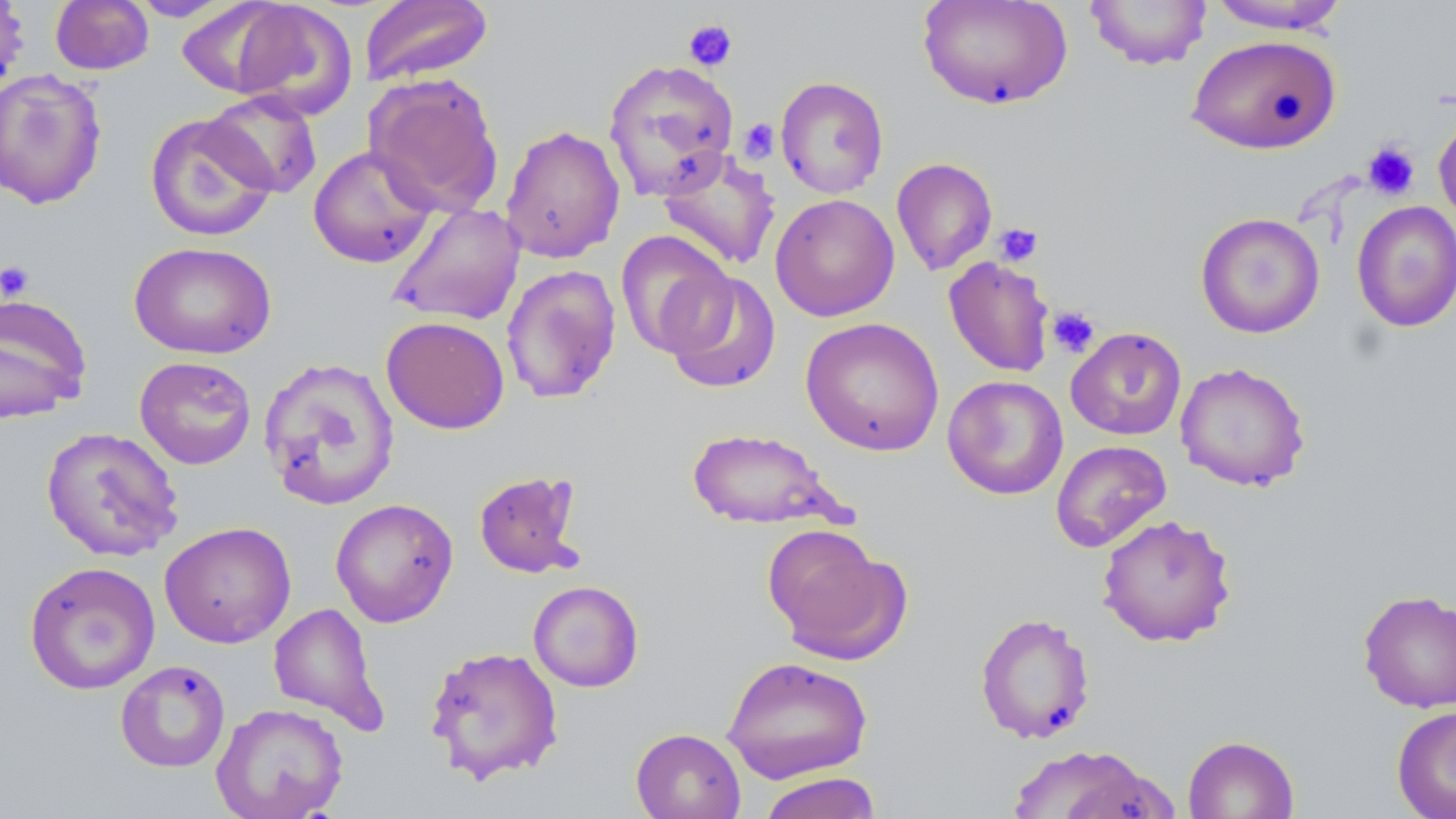
Summary:
  - Coordinate format: approximate bounding boxes as (x1, y1, x2, y2) in pixels
  - Platelet locations: (682, 19, 738, 72), (736, 118, 780, 161), (1362, 141, 1420, 201), (993, 223, 1044, 267), (0, 260, 35, 303), (1046, 306, 1100, 359)
  - Uninfected red blood cell locations: (50, 0, 154, 75), (127, 0, 238, 21), (359, 0, 494, 87), (918, 0, 1073, 110), (1085, 0, 1212, 70), (1205, 0, 1350, 34), (0, 1, 30, 96), (230, 1, 358, 121), (175, 2, 294, 98), (1187, 34, 1343, 154), (603, 58, 740, 201), (0, 69, 108, 210), (364, 73, 505, 218), (774, 76, 889, 199), (202, 90, 323, 198), (1433, 111, 1456, 233), (144, 112, 279, 242), (500, 124, 625, 264), (308, 144, 438, 269), (657, 149, 782, 272), (892, 157, 998, 276), (770, 193, 900, 321), (1351, 200, 1456, 333), (387, 203, 525, 326), (1195, 212, 1325, 339), (615, 230, 735, 358), (129, 240, 277, 360), (943, 256, 1055, 377), (500, 265, 621, 404), (662, 270, 782, 394), (0, 293, 92, 424), (381, 316, 510, 434), (800, 317, 944, 455), (1066, 327, 1187, 441), (134, 356, 257, 470), (258, 356, 401, 510), (1174, 362, 1311, 491), (942, 375, 1068, 500), (40, 426, 184, 562), (685, 426, 846, 530), (1051, 439, 1172, 552), (473, 470, 584, 579), (330, 498, 458, 627), (1096, 514, 1237, 647), (159, 521, 296, 648), (764, 527, 910, 664), (23, 560, 161, 695), (527, 580, 644, 692), (1358, 589, 1456, 713), (268, 602, 388, 734), (974, 612, 1096, 744), (424, 644, 564, 785), (721, 656, 873, 784), (114, 660, 231, 773), (211, 702, 348, 819), (1391, 705, 1456, 819), (630, 727, 746, 819), (1183, 734, 1299, 819), (1005, 744, 1166, 818), (757, 771, 882, 819)
  - Slide-level diagnosis: negative for blood parasites
  - Modality: light microscopy
  - Field of view: one of a larger specimen
  - Image size: 1456×819 pixels
  - Stain: May-Grünwald-Giemsa
  - Preparation: thin blood smear
  - Magnification: 1000x